State which parasite is depicted.
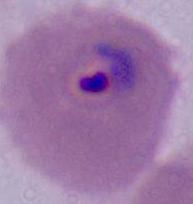

Plasmodium.

modality: micrograph
magnification: 400x or 1000x